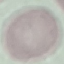
malaria status = uninfected
capture = smartphone camera at the microscope eyepiece
stain = Giemsa
image type = automatically extracted cell patch, resized to 64 × 64 pixels
preparation = thin blood film